Assess this cell for malaria.
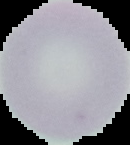

Uninfected.

Summary:
  - Preparation: thin blood film
  - Image type: segmented cell region on a black background
  - Image size: 130×145 pixels